Describe the morphology of the red blood cells.
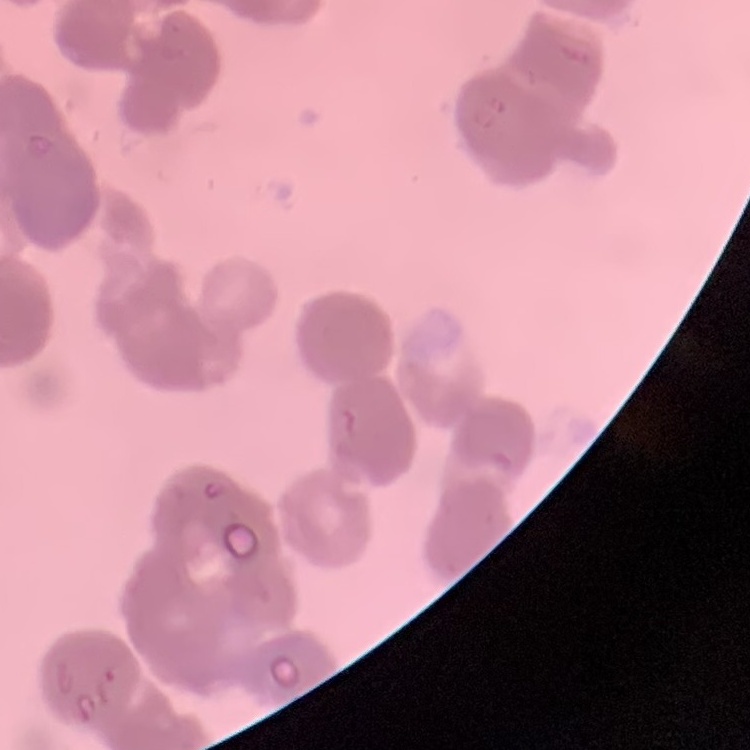

Rouleaux formation.

Thin blood smear. Field's or Giemsa stain. Square crop of a larger photomicrograph.